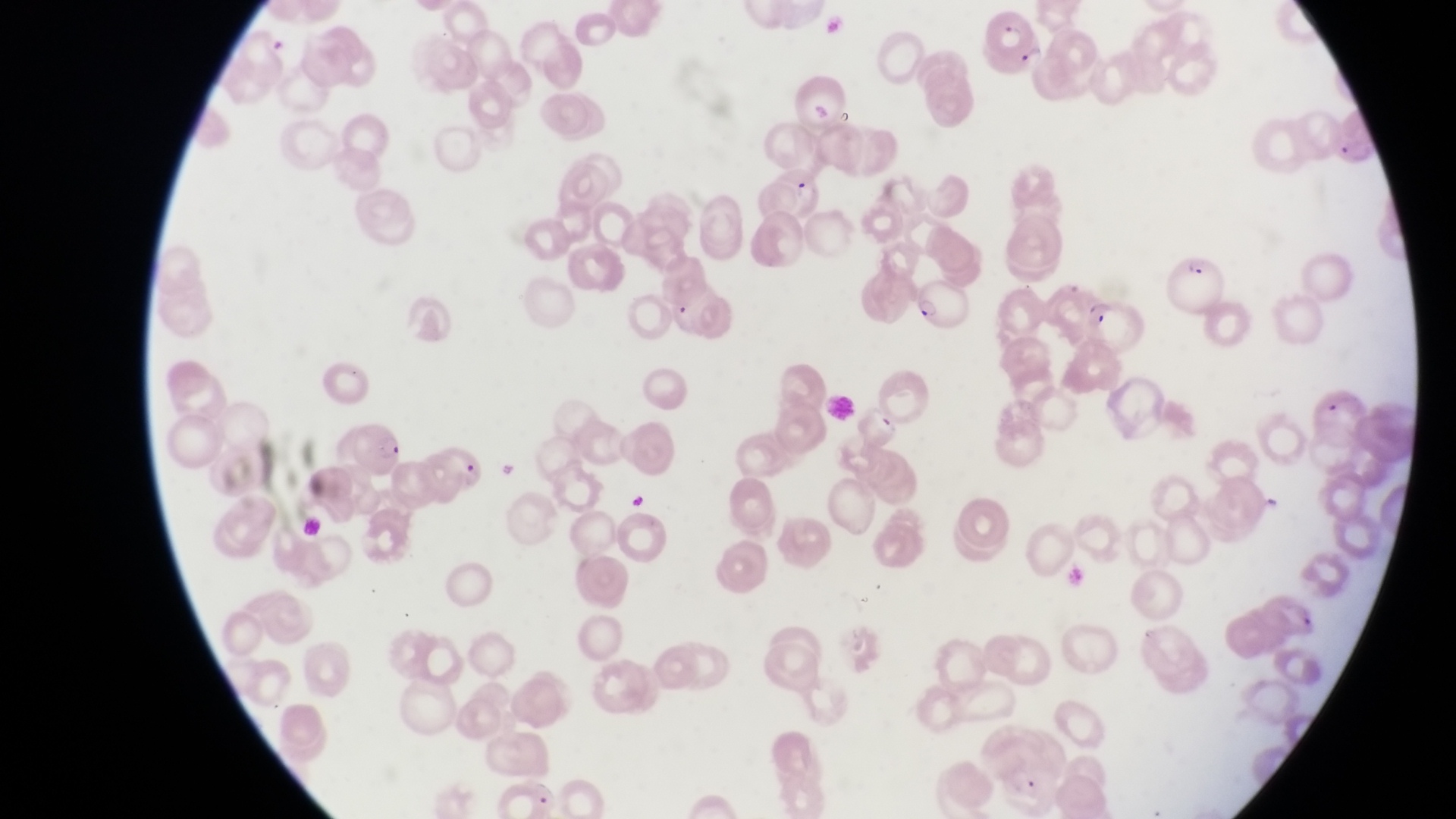

Approximate bounding boxes as {left, top, right, bottom} in pixels.
Summary:
  - Parasitised red blood cell locations: {977, 7, 1036, 60}, {1332, 111, 1382, 166}, {1169, 257, 1224, 310}, {918, 275, 976, 331}, {673, 296, 697, 326}, {1083, 300, 1154, 353}, {343, 422, 403, 474}, {441, 444, 491, 496}
  - Artifact (platelet-like body, stain precipitate, or debris) locations: {783, 172, 817, 204}, {624, 488, 654, 514}
  - Trophozoite locations: {1255, 488, 1284, 517}
  - Image size: 1456×819 pixels
  - Capture: smartphone photograph through the eyepiece of an Olympus CX-23 microscope
  - Magnification: 1000x
  - Field of view: single
  - Preparation: thin blood film
  - Country: Uganda